Name the cell type shown.
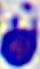

This is a leukocyte.

{
  "modality": "photomicrograph",
  "magnification": "400x"
}